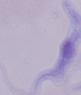

A trypanosome is seen. 1000x magnification. Micrograph.